Identify the cell.
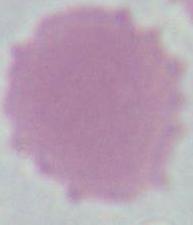

This is an erythrocyte.

1000x magnification. Photomicrograph.